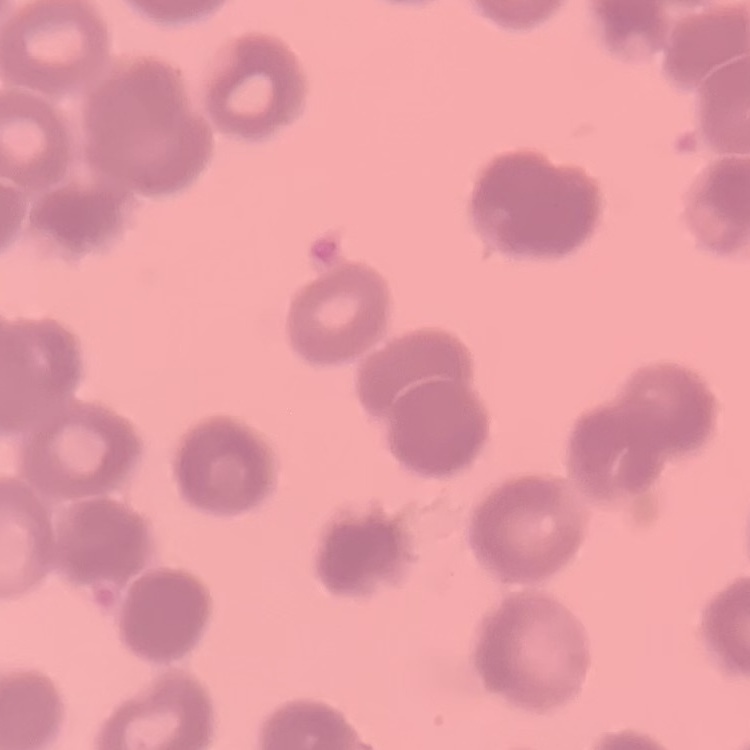
The erythrocytes show rouleaux formation. Field's or Giemsa stain. Thin blood smear. One tile cut from a larger photomicrograph.